State the blood parasite species.
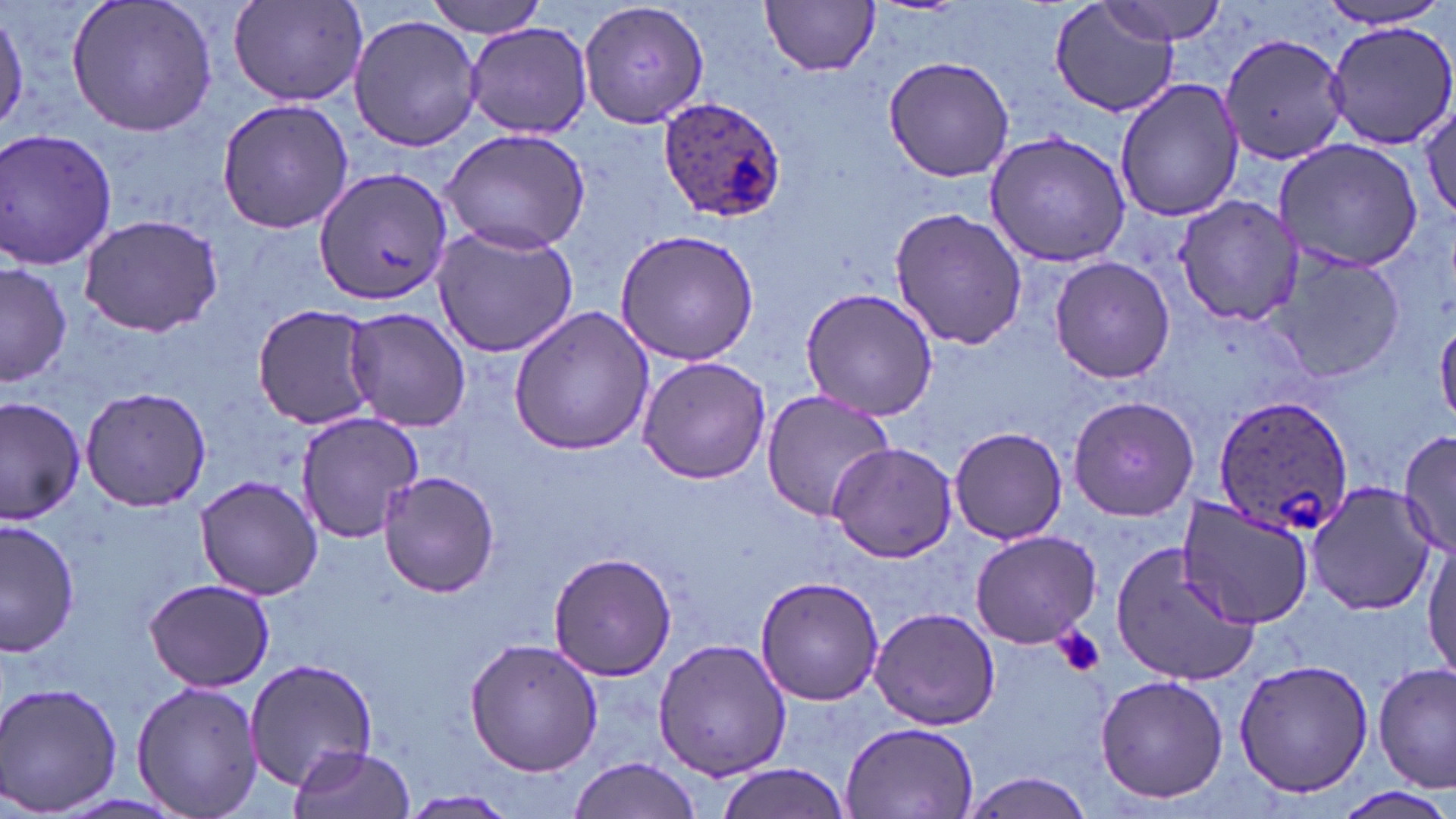
Plasmodium ovale.

Summary:
  - Coordinate format: approximate bounding boxes as (x1,y1)-(x2,y2) corner pairs in pixels
  - Platelet locations: (1052,626)-(1106,678)
  - Plasmodium ovale-infected red blood cell locations: (656,98)-(787,223), (1213,396)-(1356,538)
  - Uninfected red blood cell locations: (65,0)-(220,139), (226,0)-(369,107), (425,0)-(553,38), (762,0)-(880,77), (1096,1)-(1232,45), (578,2)-(709,130), (1311,2)-(1454,31), (1049,3)-(1179,118), (347,13)-(482,154), (1325,19)-(1456,151), (466,24)-(591,139), (1220,33)-(1353,169), (883,55)-(1015,183), (1114,78)-(1245,223), (213,95)-(356,235), (1420,95)-(1454,231), (439,125)-(592,254), (1,129)-(118,271), (984,131)-(1133,268), (1274,137)-(1427,273), (313,168)-(451,306), (1171,192)-(1304,326), (888,206)-(1028,350), (74,212)-(224,337), (429,224)-(579,358), (611,228)-(762,366), (1272,252)-(1402,385), (1048,256)-(1175,384), (0,261)-(72,389), (798,285)-(939,422), (250,303)-(379,429), (507,305)-(657,457), (342,306)-(473,431), (635,354)-(771,484), (79,385)-(215,512), (759,389)-(895,523), (1067,394)-(1202,521), (1,395)-(86,524), (293,409)-(427,544), (948,426)-(1067,545), (1397,428)-(1456,562), (826,441)-(960,564), (378,469)-(502,597), (194,476)-(325,600), (1307,483)-(1435,616), (1176,495)-(1317,628), (0,518)-(78,660), (970,530)-(1102,647), (1110,539)-(1265,687), (1424,541)-(1456,678), (548,551)-(678,681), (754,574)-(885,705), (144,578)-(274,693), (868,605)-(1002,731), (653,637)-(790,781), (463,639)-(603,777), (243,656)-(383,795), (1232,657)-(1377,799), (1373,663)-(1455,793), (1093,675)-(1230,805), (130,678)-(264,819), (0,682)-(125,816), (840,722)-(979,817), (287,744)-(417,819), (567,758)-(705,818), (714,764)-(850,819), (959,771)-(1097,818), (1341,785)-(1452,819), (396,791)-(519,818)
  - Preparation: thin blood smear
  - Stain: May-Grünwald-Giemsa
  - Modality: light microscopy
  - Field of view: one of a larger specimen
  - Magnification: 1000x
  - Image size: 1456×819 pixels